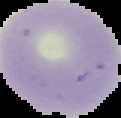 Result: no Plasmodium parasites seen. Segmented cell region on a black background. From a thin blood smear. Image is 121×118 pixels.